Outline each blood parasite and name the species.
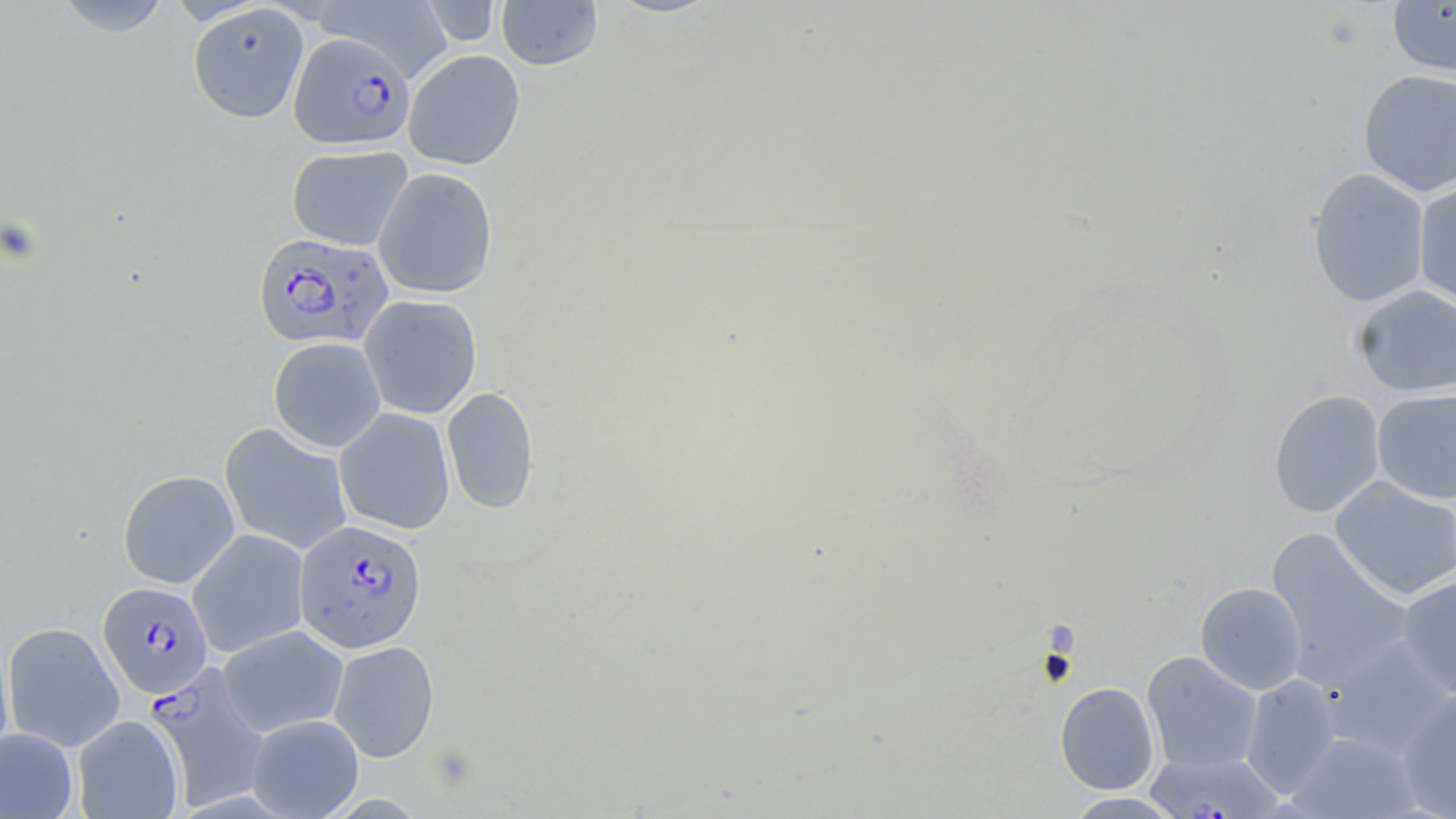
Approximate bounding boxes as named x1/y1/x2/y2 corners in pixels.
Plasmodium falciparum-infected red blood cells (subset): (x1=289, y1=33, x2=415, y2=150), (x1=253, y1=232, x2=394, y2=350), (x1=294, y1=519, x2=427, y2=653), (x1=98, y1=581, x2=213, y2=698), (x1=145, y1=663, x2=270, y2=810).
No Plasmodium ovale, Plasmodium malariae, Plasmodium vivax, Babesia divergens, or Trypanosoma brucei observed.

slide-level diagnosis = Plasmodium falciparum
image size = 1456×819 pixels
preparation = thin blood smear
field of view = single
stain = May-Grünwald-Giemsa
magnification = 1000x
modality = optical microscopy
uninfected red blood cell locations (subset) = approximate bounding boxes as named x1/y1/x2/y2 corners in pixels: (x1=52, y1=0, x2=174, y2=37), (x1=314, y1=0, x2=454, y2=82), (x1=496, y1=0, x2=603, y2=71), (x1=1387, y1=0, x2=1456, y2=76), (x1=421, y1=1, x2=502, y2=47), (x1=188, y1=3, x2=309, y2=123), (x1=403, y1=50, x2=525, y2=170), (x1=1358, y1=68, x2=1456, y2=197), (x1=287, y1=144, x2=413, y2=251), (x1=373, y1=167, x2=498, y2=298), (x1=1307, y1=168, x2=1431, y2=308), (x1=1413, y1=179, x2=1456, y2=311), (x1=1353, y1=284, x2=1456, y2=397), (x1=359, y1=294, x2=482, y2=419), (x1=268, y1=337, x2=386, y2=452), (x1=442, y1=386, x2=540, y2=515), (x1=1372, y1=388, x2=1456, y2=504), (x1=1268, y1=389, x2=1385, y2=518), (x1=334, y1=407, x2=455, y2=535), (x1=117, y1=469, x2=240, y2=588), (x1=1330, y1=476, x2=1456, y2=601), (x1=188, y1=529, x2=310, y2=658), (x1=1266, y1=530, x2=1414, y2=689), (x1=1396, y1=575, x2=1456, y2=699), (x1=1195, y1=581, x2=1306, y2=695), (x1=2, y1=621, x2=125, y2=752), (x1=218, y1=625, x2=348, y2=738), (x1=0, y1=628, x2=16, y2=766), (x1=1323, y1=635, x2=1455, y2=760), (x1=329, y1=640, x2=440, y2=762), (x1=1141, y1=651, x2=1263, y2=774), (x1=1240, y1=674, x2=1341, y2=799), (x1=1055, y1=681, x2=1159, y2=795), (x1=1397, y1=688, x2=1456, y2=818), (x1=246, y1=714, x2=364, y2=819), (x1=72, y1=715, x2=184, y2=818), (x1=0, y1=727, x2=78, y2=818), (x1=1288, y1=732, x2=1422, y2=818), (x1=1143, y1=752, x2=1285, y2=818), (x1=1062, y1=792, x2=1187, y2=818)